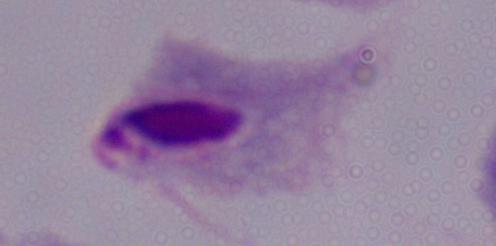
modality = micrograph
identification = trichomonad
magnification = 1000x